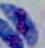

Summary:
  - Identification: Toxoplasma gondii
  - Magnification: 1000x
  - Modality: photomicrograph